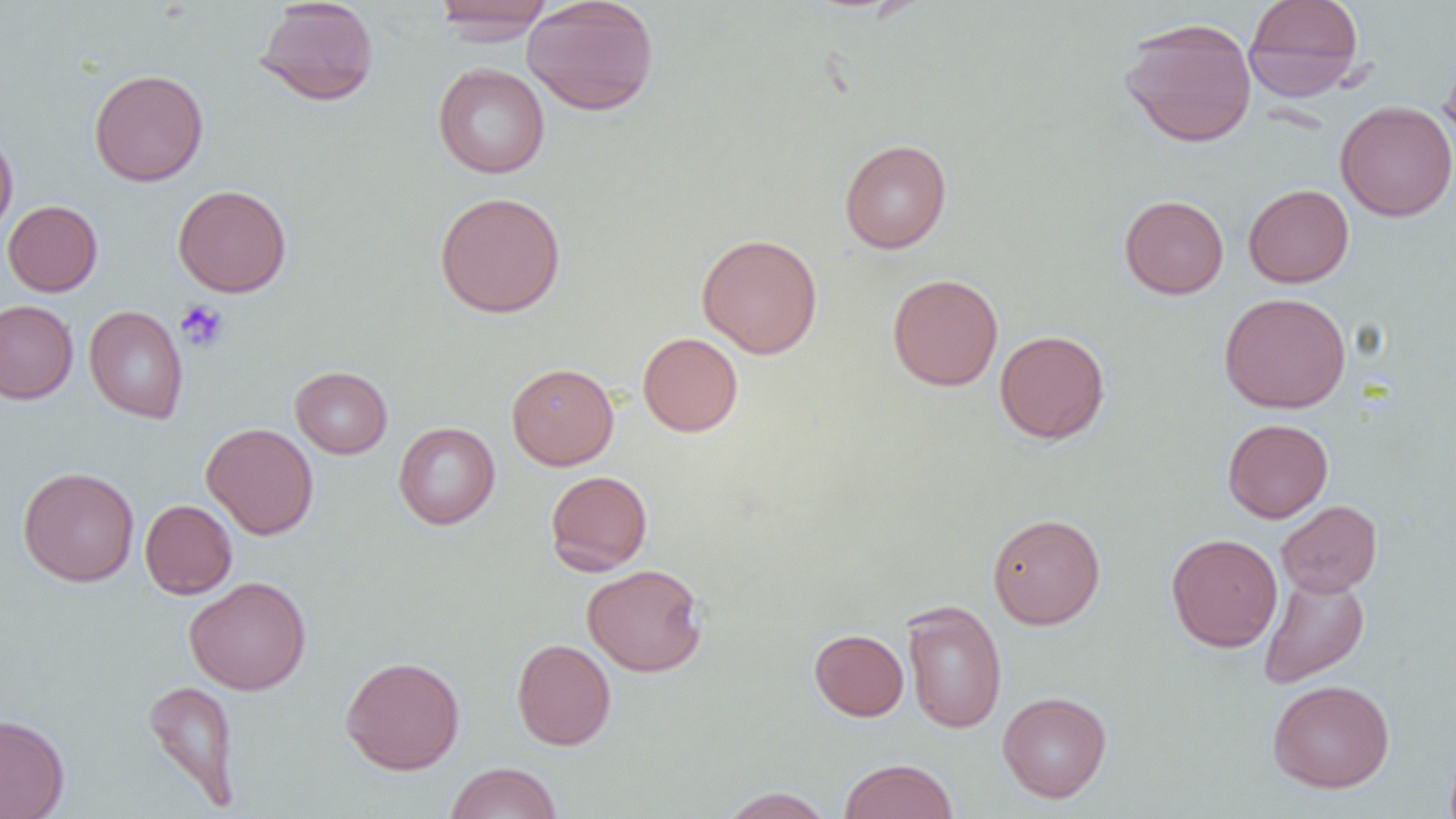

Approximate bounding boxes as (x1, y1, x2, y2) in pixels. Uninfected red blood cell locations: (254, 0, 379, 106), (521, 0, 659, 116), (1243, 0, 1364, 102), (431, 1, 555, 41), (1119, 17, 1257, 148), (1438, 47, 1456, 157), (432, 62, 550, 178), (88, 68, 209, 186), (1335, 101, 1456, 222), (0, 126, 19, 240), (839, 139, 952, 253), (172, 184, 292, 297), (1243, 184, 1355, 287), (434, 191, 566, 318), (1119, 195, 1229, 299), (2, 200, 103, 296), (697, 233, 823, 359), (887, 273, 1003, 391), (1219, 292, 1351, 413), (0, 300, 78, 404), (84, 305, 189, 423), (994, 330, 1110, 444), (637, 332, 743, 437), (506, 362, 619, 469), (290, 366, 392, 459), (1222, 418, 1333, 522), (393, 422, 500, 529), (201, 423, 319, 539), (17, 466, 139, 587), (545, 470, 653, 576), (139, 499, 237, 599), (1275, 500, 1382, 597), (987, 513, 1105, 629), (1166, 533, 1283, 652), (582, 563, 707, 677), (1258, 574, 1369, 688), (184, 576, 312, 695), (901, 600, 1008, 734), (810, 628, 908, 721), (512, 638, 616, 750), (340, 655, 465, 775), (1267, 679, 1395, 793), (143, 680, 241, 811), (997, 691, 1112, 802), (0, 713, 69, 819), (839, 758, 958, 819), (445, 762, 561, 819), (718, 787, 834, 819). Platelet locations: (174, 300, 229, 353). Slide-level diagnosis: negative for blood parasites. Thin blood film. Image is 1456×819 pixels. Light microscopy. 1000x magnification. Single field of view.